Name the parasite shown.
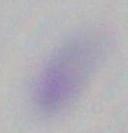

This is Toxoplasma gondii.

modality = micrograph
magnification = 1000x